Outline each blood parasite and name the species.
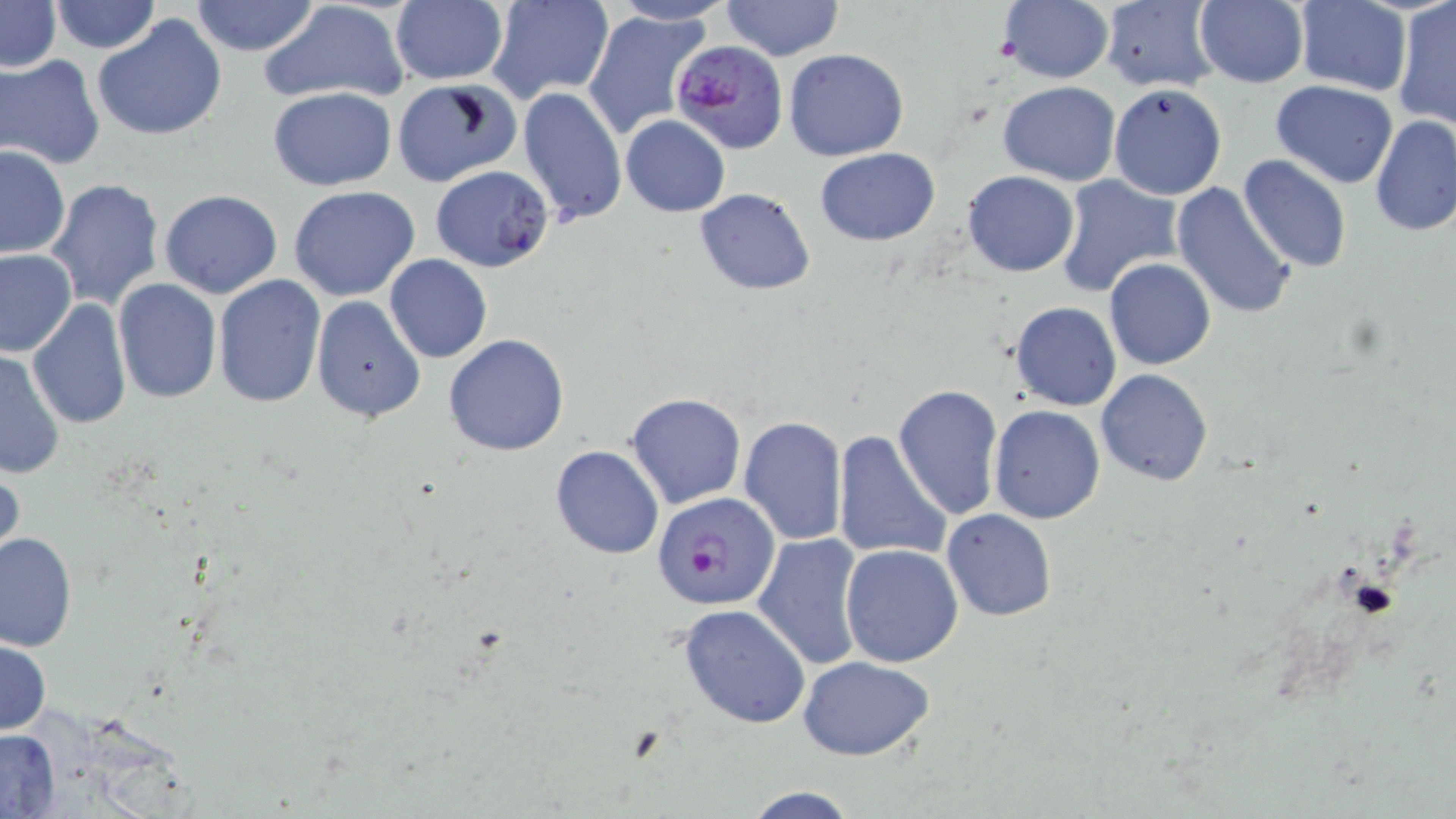
Approximate bounding boxes as (x1,y1)-(x2,y2) corner pairs in pixels.
Plasmodium falciparum-infected red blood cells: (671,39)-(788,156), (652,491)-(781,610).
No Plasmodium ovale, Plasmodium malariae, Plasmodium vivax, Babesia divergens, or Trypanosoma brucei observed.

Summary:
  - Uninfected red blood cell locations: (1,0)-(61,73), (389,0)-(507,85), (488,0)-(616,105), (722,0)-(842,60), (996,0)-(1114,85), (1099,0)-(1221,92), (190,1)-(320,56), (261,1)-(411,108), (607,1)-(737,25), (1193,1)-(1309,87), (1296,1)-(1411,97), (50,2)-(160,54), (1392,2)-(1456,130), (583,10)-(714,141), (92,15)-(227,141), (784,49)-(909,161), (0,54)-(105,169), (392,79)-(521,186), (1270,79)-(1398,188), (998,80)-(1121,185), (1109,83)-(1226,200), (518,86)-(627,229), (267,87)-(397,190), (621,115)-(730,217), (1371,116)-(1456,236), (0,146)-(71,260), (814,146)-(940,245), (1238,154)-(1352,273), (429,164)-(555,272), (962,171)-(1079,276), (1055,175)-(1183,295), (46,177)-(165,311), (1170,180)-(1297,321), (289,185)-(421,301), (159,189)-(283,298), (695,189)-(817,294), (0,248)-(77,358), (386,255)-(492,363), (1104,258)-(1217,370), (212,275)-(325,408), (113,278)-(221,403), (312,297)-(425,424), (1010,301)-(1121,411), (27,302)-(132,430), (443,334)-(570,456), (0,350)-(67,481), (1096,368)-(1212,488), (894,384)-(1003,520), (626,392)-(746,509), (989,405)-(1106,524), (738,416)-(848,543), (570,426)-(733,548), (832,430)-(953,565), (550,444)-(665,561), (0,463)-(24,571), (942,509)-(1056,621), (0,530)-(77,653), (753,532)-(865,671), (841,544)-(964,666), (679,603)-(811,728), (0,636)-(51,737), (797,656)-(934,761), (0,729)-(61,816), (738,784)-(864,819)
  - Slide-level diagnosis: Plasmodium falciparum
  - Field of view: single
  - Magnification: 1000x
  - Preparation: thin blood film
  - Modality: optical microscopy
  - Stain: May-Grünwald-Giemsa
  - Image size: 1456×819 pixels